Locate and identify every blood parasite.
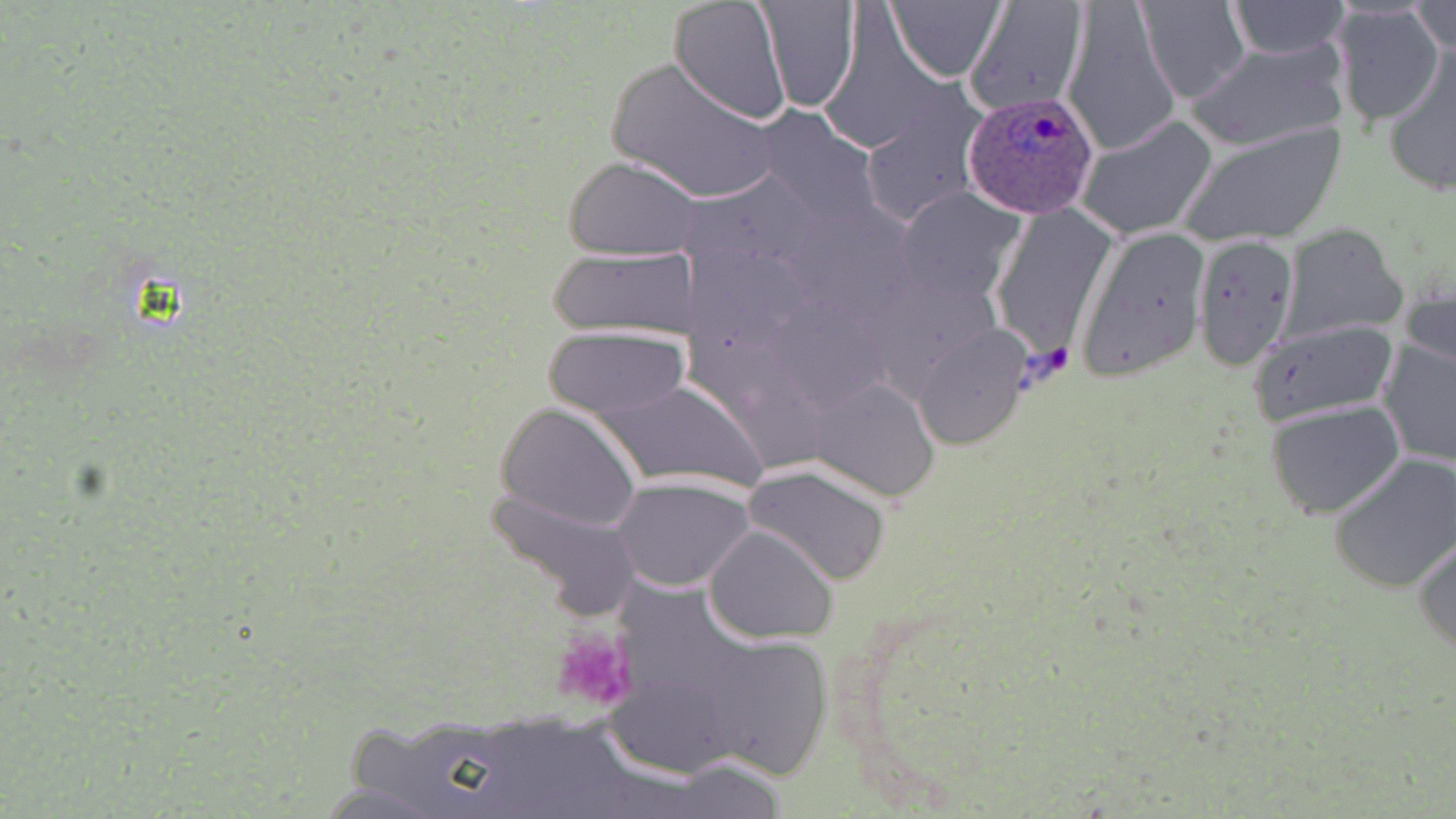
Approximate bounding boxes as named x1/y1/x2/y2 corners in pixels.
Plasmodium ovale-infected red blood cells: (x1=962, y1=92, x2=1098, y2=219).
No Plasmodium falciparum, Plasmodium malariae, Plasmodium vivax, Babesia divergens, or Trypanosoma brucei observed.

slide_level_diagnosis: Plasmodium ovale
uninfected_red_blood_cell_locations: 'approximate bounding boxes as named x1/y1/x2/y2 corners in pixels: (x1=668, y1=0, x2=792, y2=125), (x1=759, y1=0, x2=863, y2=112), (x1=887, y1=0, x2=1006, y2=82), (x1=963, y1=0, x2=1090, y2=118), (x1=1136, y1=0, x2=1250, y2=104), (x1=1226, y1=0, x2=1349, y2=59), (x1=1393, y1=0, x2=1456, y2=77), (x1=1063, y1=3, x2=1179, y2=157), (x1=1331, y1=3, x2=1446, y2=129), (x1=1411, y1=3, x2=1454, y2=54), (x1=1187, y1=40, x2=1351, y2=153), (x1=1379, y1=44, x2=1456, y2=196), (x1=605, y1=55, x2=780, y2=205), (x1=857, y1=88, x2=988, y2=231), (x1=757, y1=105, x2=881, y2=227), (x1=1077, y1=116, x2=1216, y2=240), (x1=1179, y1=122, x2=1346, y2=247), (x1=565, y1=156, x2=705, y2=262), (x1=899, y1=187, x2=1023, y2=298), (x1=990, y1=204, x2=1118, y2=354), (x1=1277, y1=224, x2=1408, y2=344), (x1=1076, y1=226, x2=1211, y2=382), (x1=1192, y1=237, x2=1300, y2=371), (x1=547, y1=248, x2=701, y2=341), (x1=1401, y1=273, x2=1456, y2=377), (x1=1247, y1=316, x2=1399, y2=426), (x1=540, y1=326, x2=688, y2=417), (x1=911, y1=327, x2=1029, y2=450), (x1=1376, y1=337, x2=1454, y2=469), (x1=591, y1=378, x2=768, y2=493), (x1=812, y1=380, x2=938, y2=501), (x1=1265, y1=401, x2=1403, y2=518), (x1=496, y1=404, x2=641, y2=532), (x1=1329, y1=453, x2=1456, y2=594), (x1=744, y1=462, x2=893, y2=586), (x1=612, y1=476, x2=755, y2=591), (x1=484, y1=482, x2=645, y2=619), (x1=704, y1=525, x2=838, y2=644), (x1=1412, y1=533, x2=1456, y2=658), (x1=702, y1=633, x2=836, y2=782), (x1=661, y1=756, x2=793, y2=818)'
preparation: thin blood film
modality: optical microscopy
image_size: 1456×819 pixels
magnification: 1000x
platelet_locations: 'approximate bounding boxes as named x1/y1/x2/y2 corners in pixels: (x1=549, y1=628, x2=636, y2=713)'
field_of_view: one of a larger specimen
stain: May-Grünwald-Giemsa